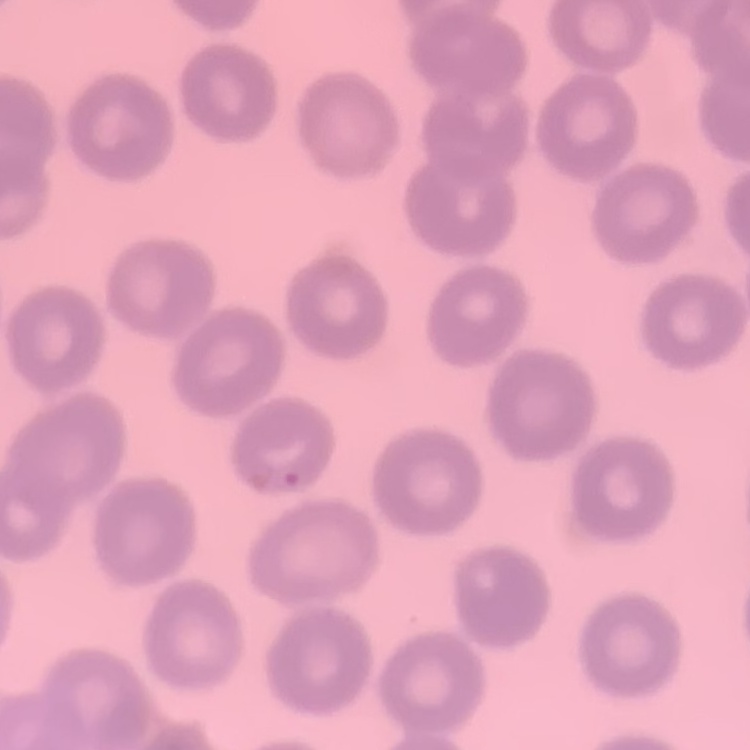
red blood cell morphology = no rouleaux formation
stain = Field's or Giemsa
preparation = thin blood smear
image type = square crop of a larger photomicrograph